Assess the morphology of the erythrocytes.
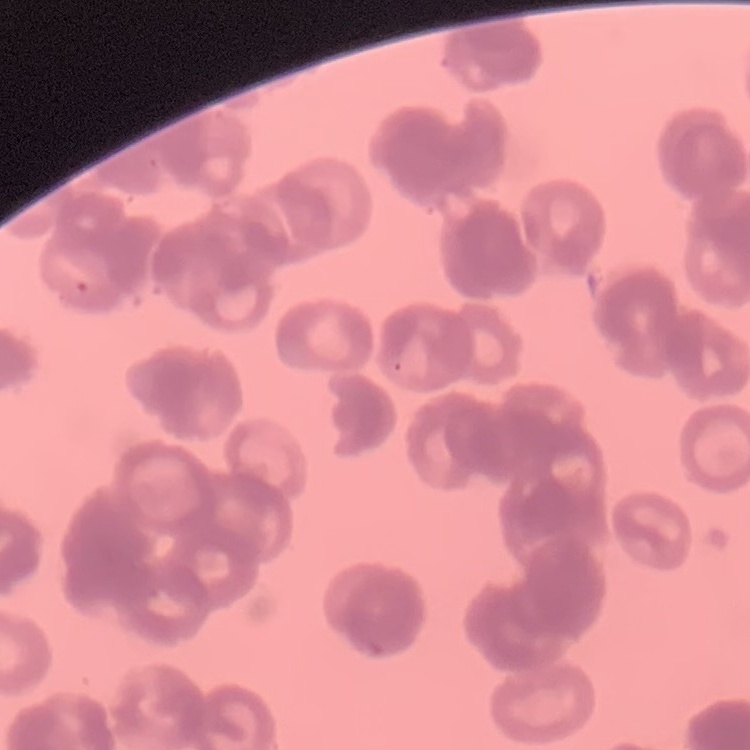
They show rouleaux formation.

Summary:
  - Preparation: thin blood film
  - Image type: one tile cut from a larger photomicrograph
  - Stain: Field's or Giemsa